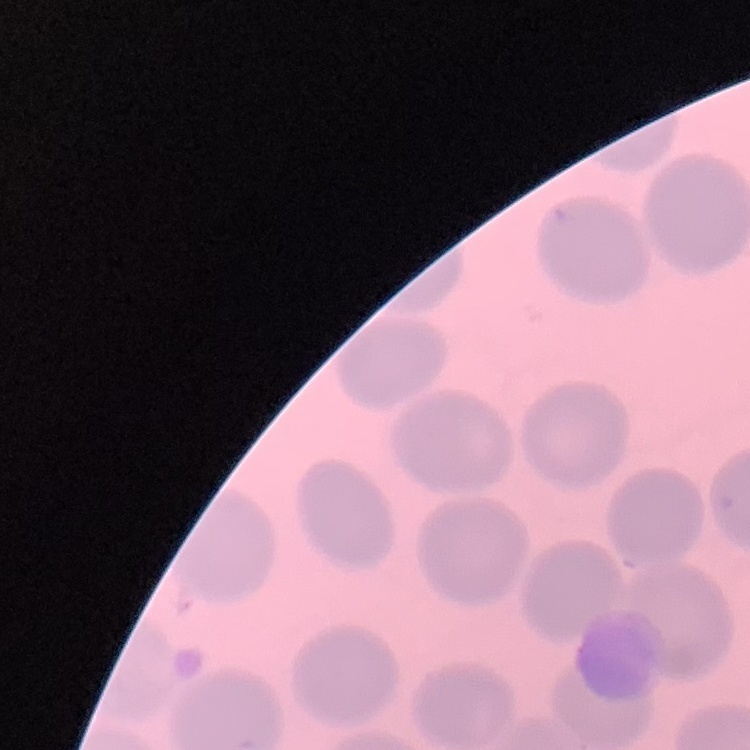 The red blood cells exhibit no rouleaux formation. One tile cut from a larger photomicrograph. Field's or Giemsa stain. Thin blood film.